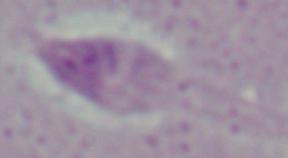
Summary:
  - Modality: micrograph
  - Identification: Leishmania
  - Magnification: 1000x